Give the extent of all uninfected red blood cells.
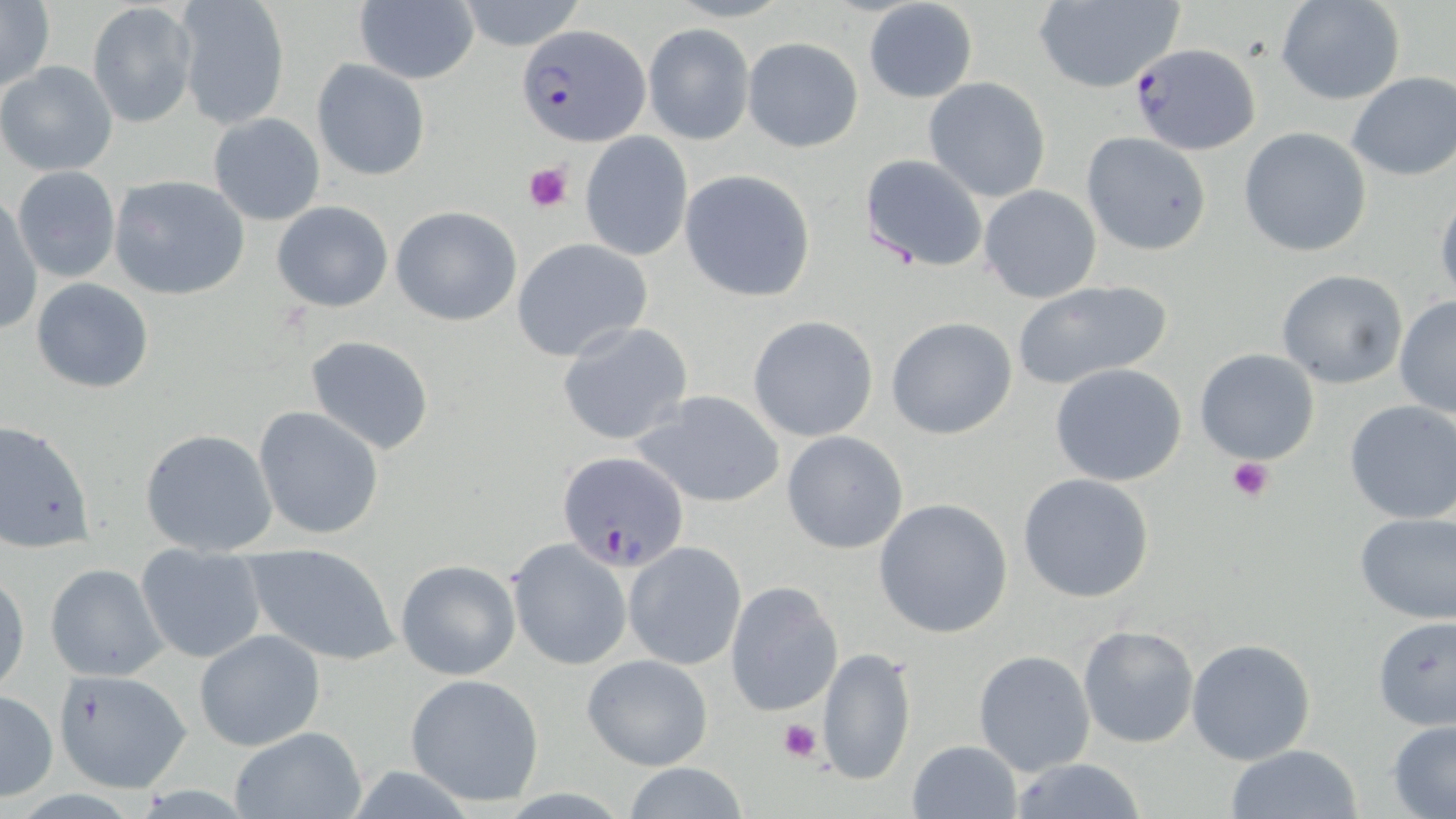
Approximate bounding boxes as (x1,y1)-(x2,y2) corner pairs in pixels.
Uninfected red blood cells: (0,0)-(54,95), (454,0)-(588,51), (1274,0)-(1406,106), (173,1)-(289,130), (1031,1)-(1187,92), (353,2)-(480,84), (862,2)-(979,104), (87,3)-(197,128), (644,24)-(753,144), (742,36)-(864,153), (312,58)-(430,181), (0,61)-(118,176), (1345,71)-(1455,182), (923,77)-(1052,203), (207,112)-(326,227), (1238,126)-(1373,257), (580,131)-(693,261), (1081,132)-(1211,255), (859,154)-(987,272), (11,164)-(121,283), (679,169)-(816,302), (109,175)-(250,300), (979,184)-(1102,304), (1434,189)-(1456,303), (1,193)-(42,337), (271,199)-(394,312), (391,205)-(522,326), (512,238)-(653,360), (1275,268)-(1407,389), (30,277)-(154,393), (1012,279)-(1177,389), (1393,296)-(1456,419), (748,314)-(878,442), (885,316)-(1019,440), (556,321)-(694,447), (303,335)-(436,455), (1193,347)-(1322,465), (1049,363)-(1188,486), (635,390)-(787,506), (1343,399)-(1456,525), (253,406)-(384,539), (0,419)-(94,553), (140,428)-(277,556), (781,430)-(908,555), (1017,474)-(1156,604), (873,498)-(1014,638), (1354,510)-(1456,626), (508,539)-(631,669), (624,541)-(747,668), (242,542)-(401,666), (136,546)-(267,664), (394,560)-(521,680), (45,563)-(168,681), (0,570)-(28,698), (727,582)-(843,717), (1372,616)-(1456,730), (1077,626)-(1200,748), (195,630)-(325,750), (1186,637)-(1317,764), (816,644)-(915,787), (973,648)-(1096,776), (580,653)-(714,771), (404,673)-(546,807), (58,678)-(196,790), (0,689)-(58,801), (1386,719)-(1456,819), (227,726)-(368,819), (907,739)-(1023,819), (1226,745)-(1365,819), (1007,758)-(1149,819), (616,762)-(757,819).

Plasmodium falciparum-infected red blood cell locations: (516,24)-(646,146), (1127,42)-(1261,156), (558,451)-(689,573). Platelet locations: (523,161)-(575,214), (1225,456)-(1275,502), (777,718)-(824,764). Slide-level diagnosis: Plasmodium falciparum. Image is 1456×819 pixels. Thin blood smear. Light microscopy. One field of a larger specimen. Captured at 1000x magnification. May-Grünwald-Giemsa-stained preparation.